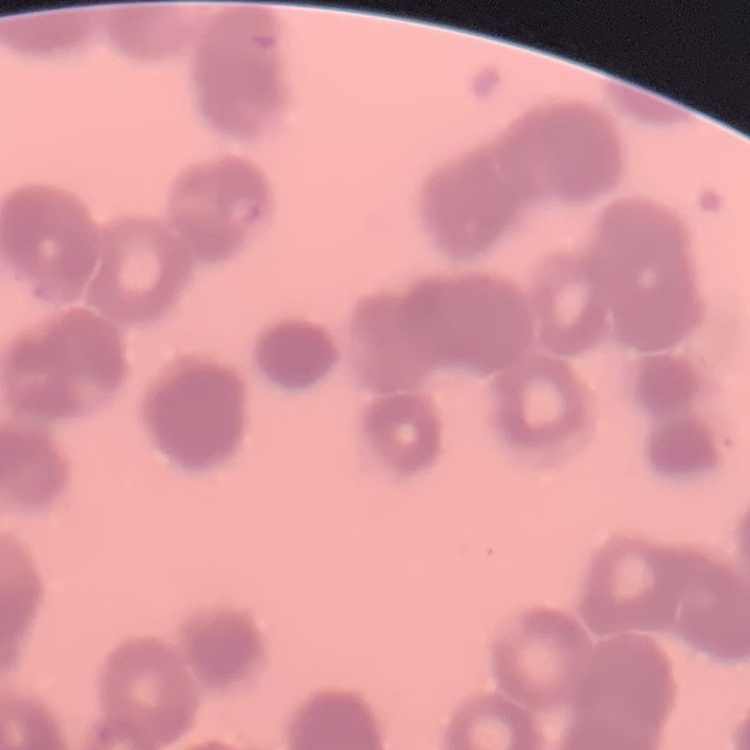

Summary:
  - Erythrocyte morphology: rouleaux formation
  - Preparation: thin blood smear
  - Image type: one tile cut from a larger photomicrograph
  - Stain: Field's or Giemsa